Give the position of every Plasmodium parasite.
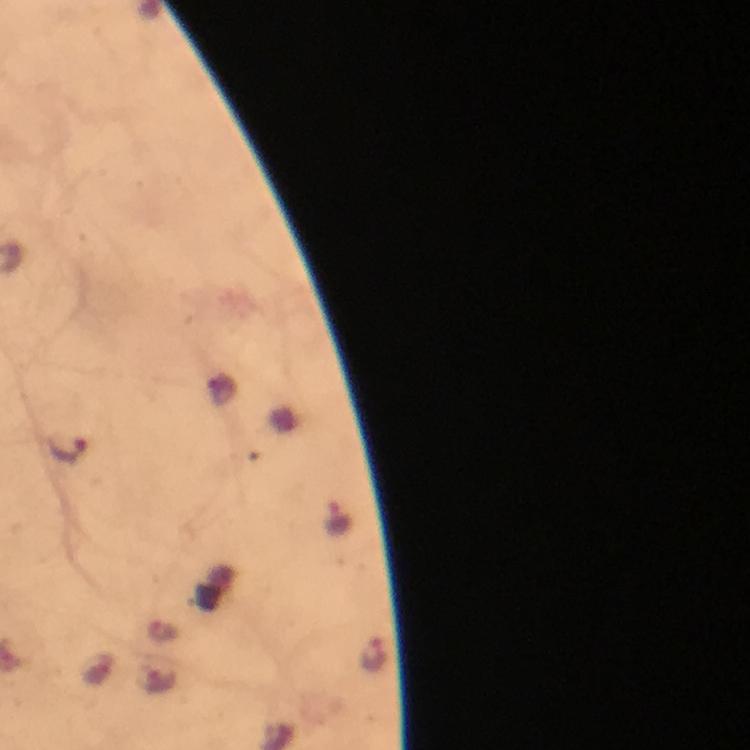
Approximate object centers, in pixels from the top-left corner.
Plasmodium parasites: (x=66, y=449), (x=337, y=520), (x=374, y=655), (x=161, y=680).

Summary:
  - Image size: 750×750 pixels
  - Capture: smartphone mounted on the microscope
  - Preparation: thick smear
  - Context: from a malaria diagnostic workup
  - Stain: Giemsa
  - Cropped from: a single field of view
  - Immersion oil: used
  - Magnification: 100x